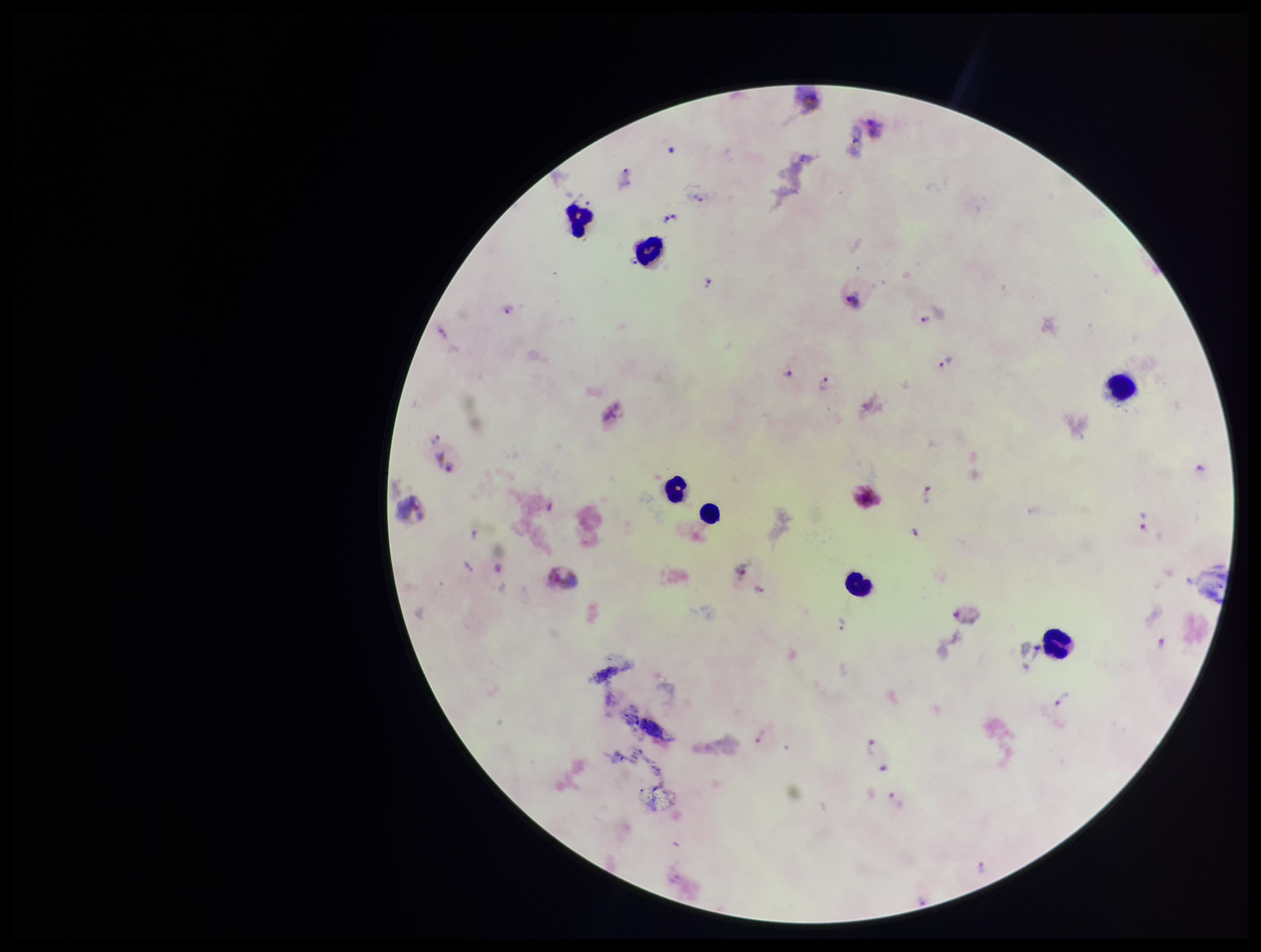

Summary:
  - Stain: Giemsa
  - Field of view: one from this slide
  - Image size: 1261×952 pixels
  - Parasite count: 20
  - Patient malaria status: positive
  - Plasmodium parasites: detected
  - Preparation: thick
  - Capture: smartphone photograph through the microscope eyepiece
  - Leukocyte count: 6
  - Species reported for this patient: Plasmodium vivax